Locate every P. falciparum parasite and identify its life-cycle stage.
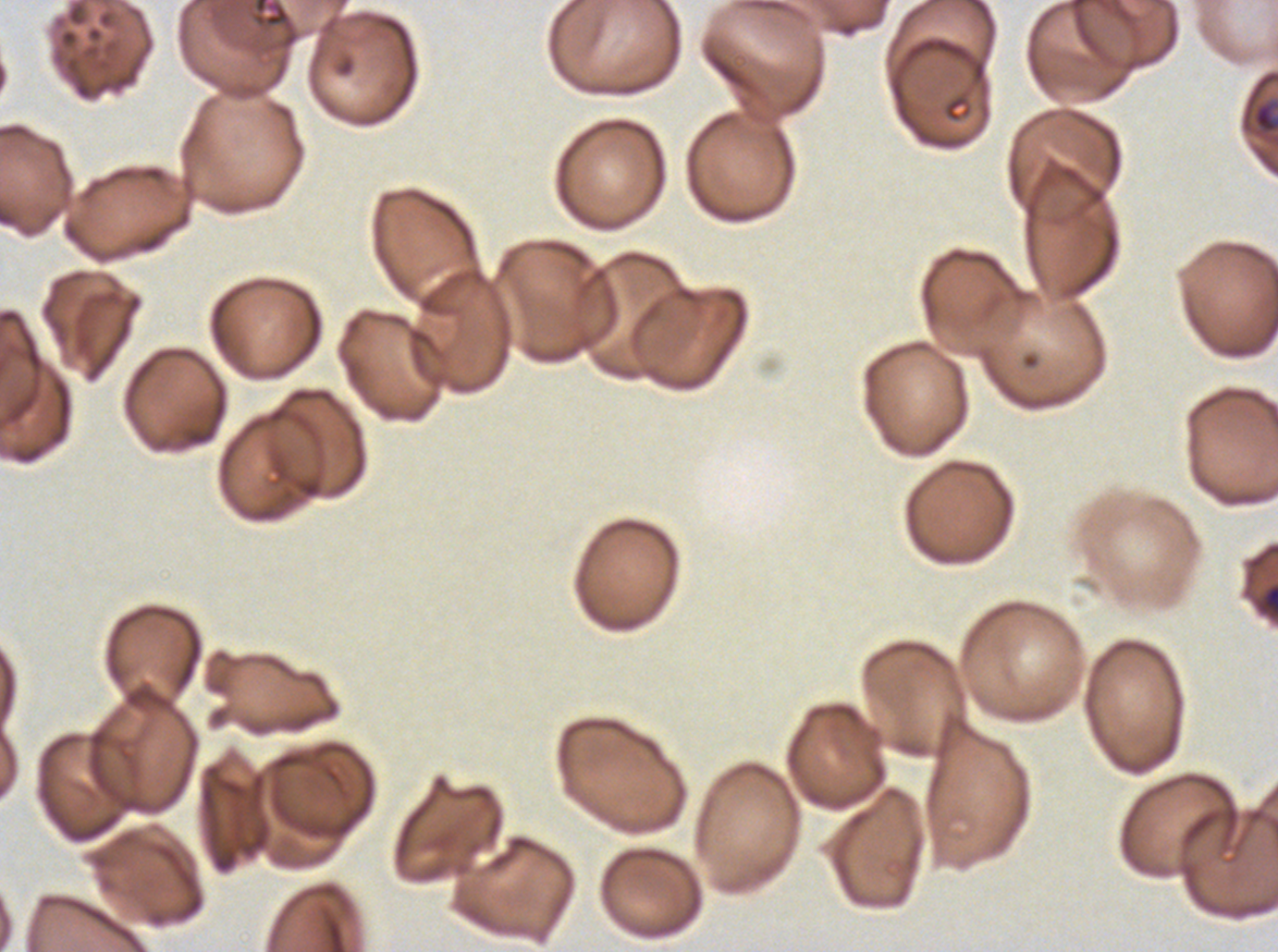
Approximate bounding boxes as {x1, y1, x2, y2} in pixels.
Rings: {1252, 100, 1277, 135}.
No late-ring/early-trophozoite forms, mid trophozoites, late trophozoites, early schizonts, late schizonts, segmenters, or gametocytes observed.

Debris locations: {1262, 583, 1277, 613}. Thin blood smear. A sub-image separated from a larger composite. Image is 1278×952 pixels. Giemsa-stained preparation. P. falciparum cultured ex vivo for 24 to 48 hours, from a patient in The Gambia.